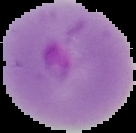
malaria_status: parasitized
preparation: thin blood film
image_type: cell region segmented out of the field of view; surrounding area masked to black
image_size: 136×133 pixels